Identify the cell.
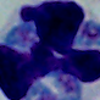
This is a leukocyte.

Micrograph. 1000x magnification.